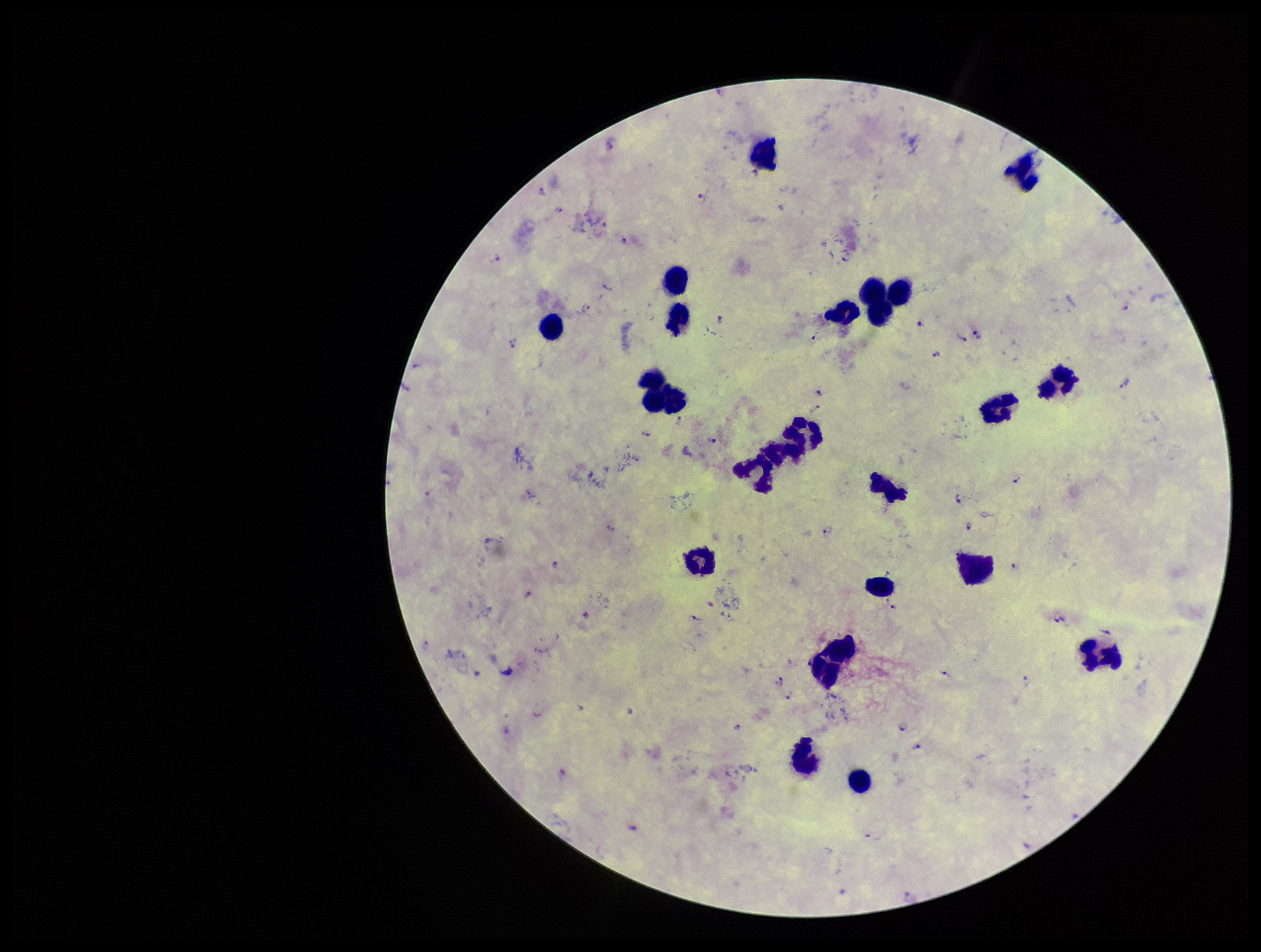

Summary:
  - Capture: smartphone photograph through the microscope eyepiece
  - Patient malaria status: positive
  - Preparation: thick smear
  - Plasmodium parasites: seen
  - Leukocyte count: 22
  - Stain: Giemsa
  - Species reported for this patient: Plasmodium falciparum
  - Parasite count: 39
  - Field of view: single
  - Image size: 1261×952 pixels